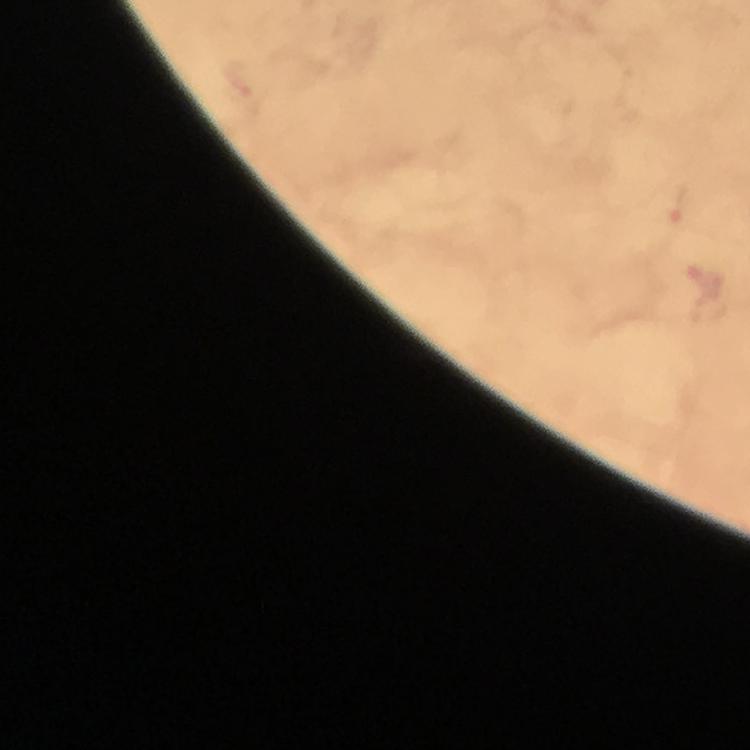

Approximate centers as (x, y) in pixels. Malaria parasite locations: (680, 207), (703, 279). A crop from one field of view. Image is 750×750 pixels. Thick blood smear. Immersion oil was used. From a diagnostic examination for malaria. Photographed with a smartphone mounted on the microscope. Giemsa-stained preparation. 100x magnification.